State which parasite is depicted.
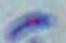
This is Toxoplasma gondii.

magnification = 1000x
modality = micrograph